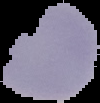

image size = 100×103 pixels
image type = segmented cell region with the area outside set to black
malaria status = uninfected
preparation = thin blood smear